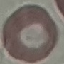

Summary:
  - Result: no malaria parasites detected
  - Preparation: thin blood smear
  - Capture: smartphone camera at the microscope eyepiece
  - Image type: cell patch, automatically extracted from a larger field of view and resized to 64 × 64 pixels
  - Stain: Giemsa